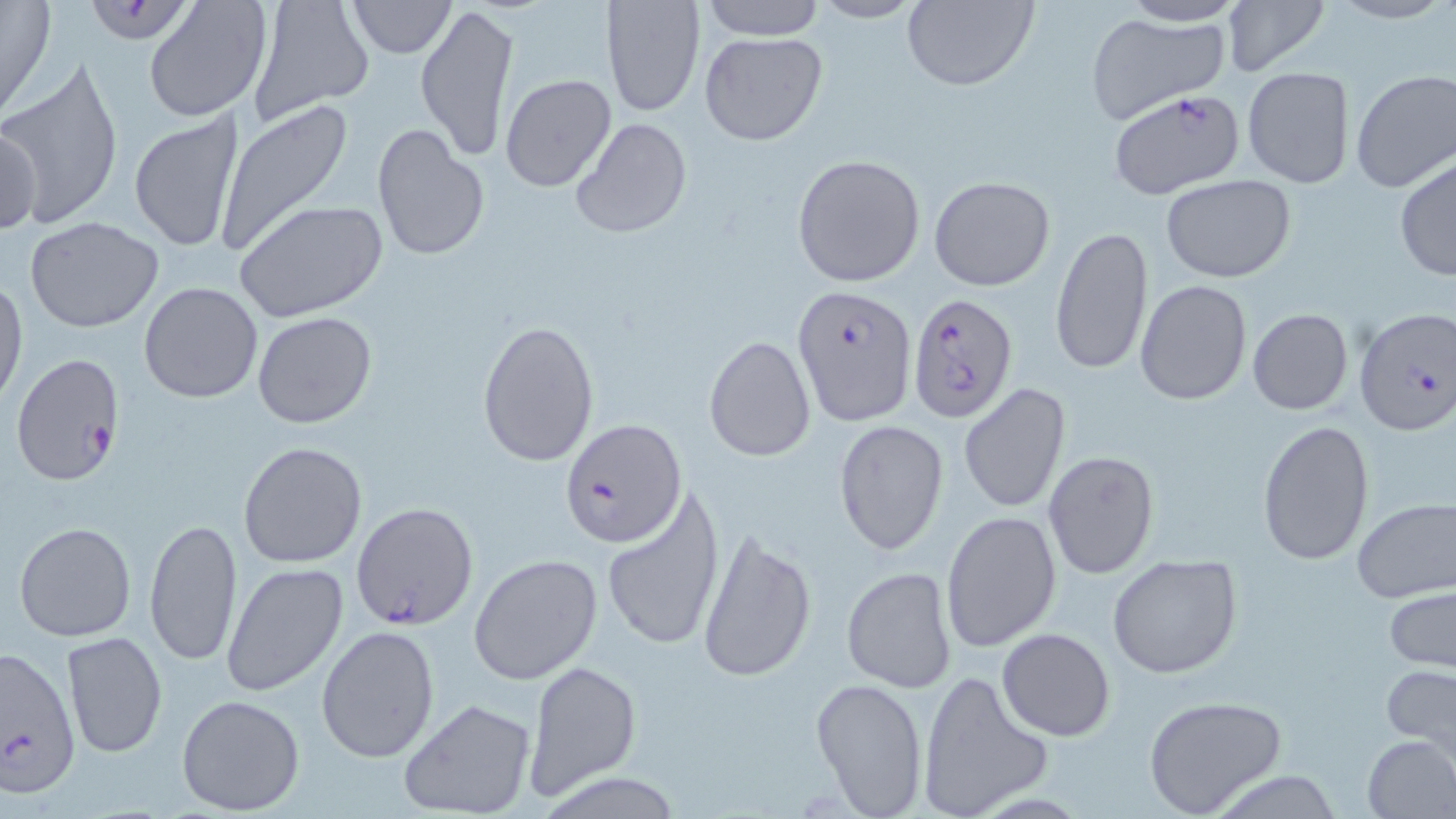
slide-level diagnosis = Plasmodium falciparum
magnification = 1000x
image size = 1456×819 pixels
field of view = single
uninfected red blood cell locations = approximate bounding boxes as [x1, y1, x2, y2] in pixels: [0, 0, 57, 121], [142, 0, 273, 124], [245, 0, 373, 127], [601, 0, 706, 117], [697, 0, 826, 41], [1220, 0, 1332, 78], [347, 1, 456, 57], [806, 1, 929, 25], [901, 1, 1039, 91], [1114, 1, 1249, 25], [414, 4, 521, 161], [1085, 11, 1231, 122], [699, 31, 828, 146], [1, 58, 126, 232], [1243, 67, 1354, 188], [1350, 68, 1456, 194], [499, 73, 617, 192], [214, 98, 355, 257], [129, 110, 249, 256], [569, 116, 694, 239], [1, 122, 41, 239], [371, 122, 490, 262], [791, 153, 927, 288], [1394, 156, 1455, 282], [928, 175, 1055, 292], [1160, 176, 1297, 282], [233, 199, 388, 322], [26, 217, 165, 332], [1049, 225, 1152, 378], [0, 277, 26, 410], [1134, 279, 1251, 407], [139, 281, 265, 403], [1246, 307, 1354, 414], [252, 312, 377, 429], [477, 319, 600, 468], [704, 332, 816, 462], [958, 383, 1071, 513], [834, 419, 949, 555], [1256, 419, 1375, 568], [238, 441, 368, 568], [1043, 451, 1159, 578], [600, 486, 724, 654], [1352, 498, 1456, 602], [941, 510, 1063, 653], [144, 516, 243, 666], [14, 522, 136, 642], [695, 528, 817, 684], [468, 554, 605, 686], [1106, 554, 1243, 678], [222, 563, 347, 698], [841, 565, 959, 694], [1384, 587, 1456, 673], [315, 625, 439, 764], [997, 628, 1115, 741], [62, 631, 167, 760], [523, 659, 640, 801], [1382, 663, 1456, 752], [917, 671, 1051, 818], [810, 675, 930, 817], [175, 693, 306, 815], [1142, 694, 1286, 817], [397, 697, 537, 819], [1361, 734, 1455, 818]
preparation = thin blood smear
stain = May-Grünwald-Giemsa
modality = optical microscopy
Plasmodium falciparum-infected red blood cell locations = approximate bounding boxes as [x1, y1, x2, y2] in pixels: [88, 1, 194, 44], [1107, 90, 1247, 200], [794, 285, 914, 423], [907, 293, 1019, 424], [1355, 307, 1456, 437], [10, 355, 125, 486], [560, 418, 689, 548], [351, 502, 478, 631], [0, 645, 80, 797]